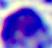

Summary:
  - Modality: micrograph
  - Identification: white blood cell
  - Magnification: 400x